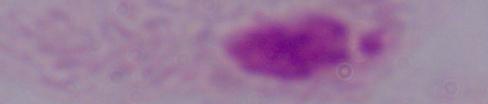
Summary:
  - Modality: photomicrograph
  - Magnification: 1000x
  - Identification: trichomonad